Report the malaria status of this cell.
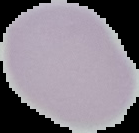
Uninfected.

image size = 139×133 pixels
image type = segmented cell region on a black background
preparation = thin blood film